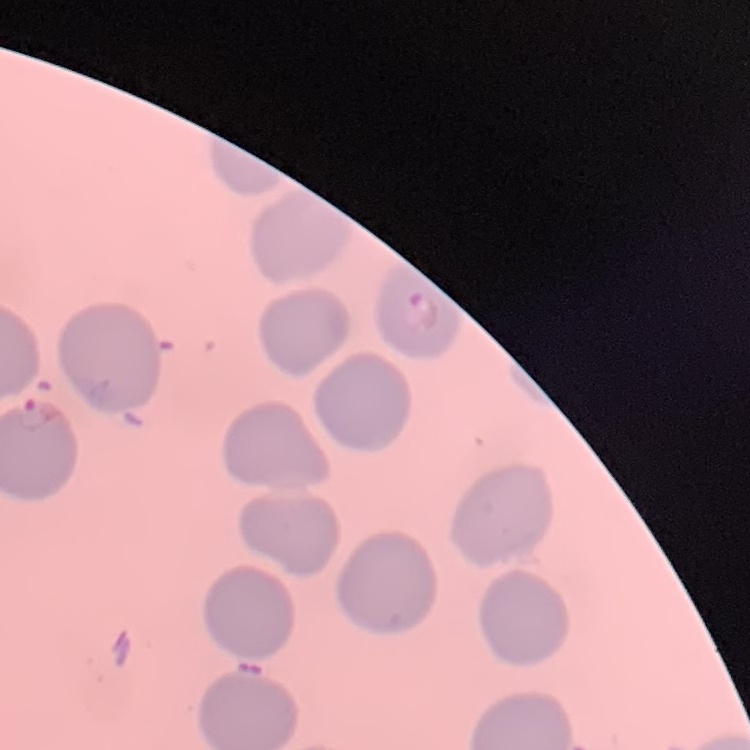

{
  "red_blood_cell_morphology": "no rouleaux formation",
  "preparation": "thin blood film",
  "image_type": "square crop of a larger photomicrograph",
  "stain": "Field's or Giemsa"
}